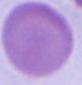
An erythrocyte is shown. Photomicrograph. Captured at 1000x magnification.